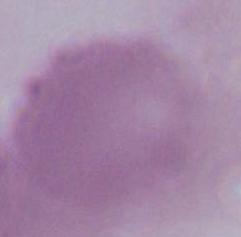

1000x magnification. An erythrocyte is shown. Photomicrograph.